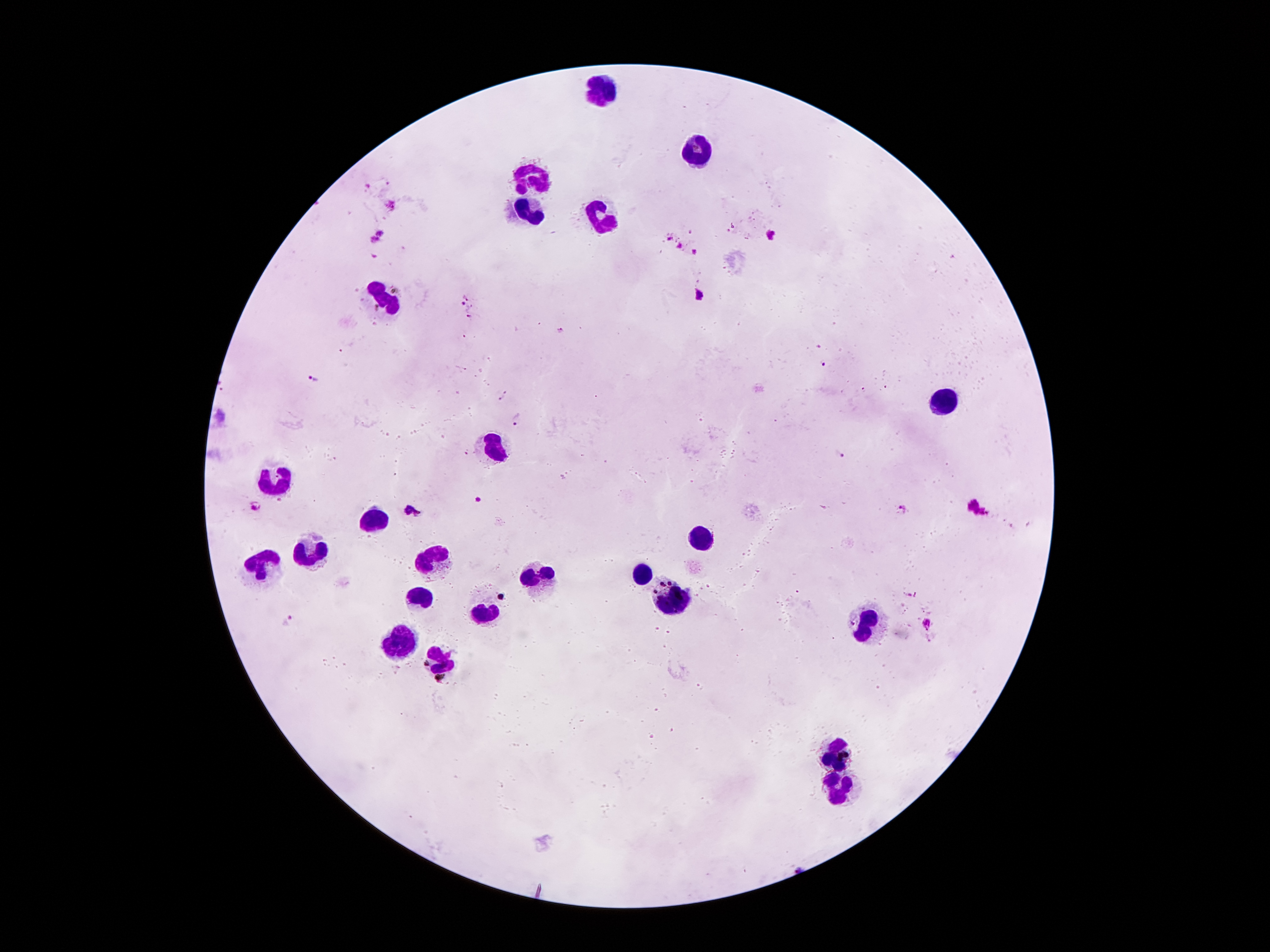 Approximate centers as (x, y) in pixels. Leukocyte locations: (600, 91), (699, 150), (527, 175), (529, 212), (602, 212), (383, 300), (945, 404), (494, 449), (277, 477), (376, 515), (704, 543), (312, 548), (434, 557), (264, 566), (640, 572), (536, 579), (416, 594), (668, 594), (485, 610), (865, 623), (399, 639), (438, 665), (834, 751), (838, 789). Plasmodium parasite locations: (689, 231), (382, 232), (773, 235), (670, 239), (374, 241), (680, 246), (695, 253), (700, 294), (465, 297), (463, 304), (469, 316), (561, 330), (822, 363), (313, 379), (502, 397), (518, 418), (841, 455), (478, 498), (413, 509), (902, 509), (256, 510), (977, 510), (288, 620), (927, 626). Giemsa stain. Patient malaria status: infected with Plasmodium falciparum. Thick blood film. 100x magnification. Image is 1270×952 pixels. One field from this slide. Photographed through the microscope eyepiece with a smartphone camera.